Locate every blood parasite and identify its species.
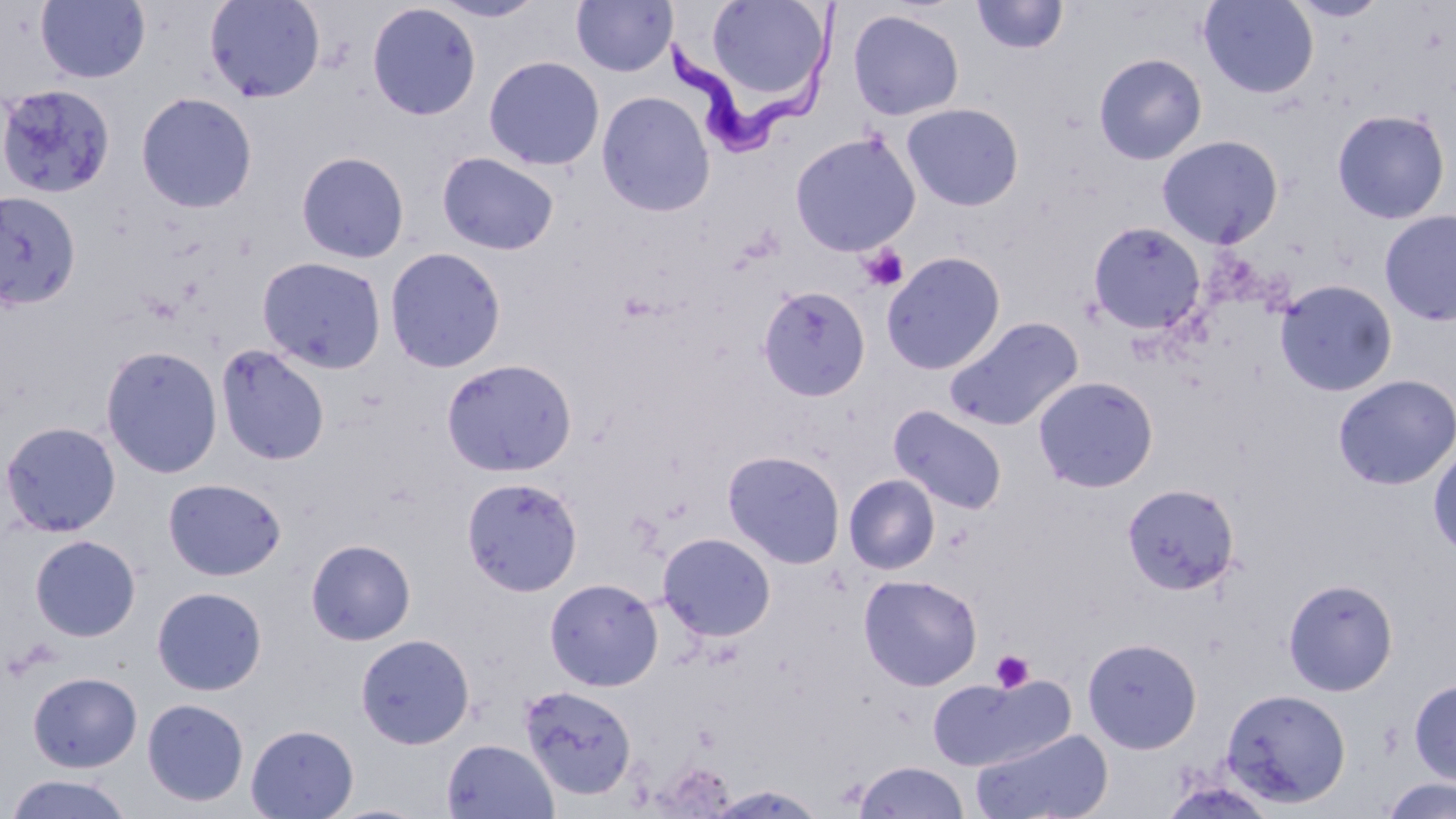

Approximate bounding boxes as (x1,y1)-(x2,y2) corner pairs in pixels.
Trypanosoma brucei: (662,2)-(849,161).
No Plasmodium falciparum, Plasmodium ovale, Plasmodium malariae, Plasmodium vivax, or Babesia divergens observed.

Summary:
  - Platelet locations: (859,244)-(909,292), (990,650)-(1034,692)
  - Uninfected red blood cell locations: (36,0)-(150,84), (204,0)-(326,103), (430,0)-(548,23), (702,0)-(831,108), (970,0)-(1069,55), (1199,0)-(1319,98), (570,1)-(676,77), (366,3)-(482,121), (846,9)-(965,121), (1093,53)-(1208,164), (484,56)-(605,171), (8,84)-(115,187), (596,91)-(716,217), (136,92)-(257,213), (901,103)-(1024,211), (1332,109)-(1450,224), (789,131)-(921,256), (1157,135)-(1283,249), (296,151)-(410,264), (436,152)-(560,256), (0,190)-(82,310), (1379,209)-(1456,326), (1087,221)-(1205,335), (384,247)-(506,373), (881,251)-(1006,375), (257,256)-(387,373), (1274,279)-(1398,397), (758,285)-(871,402), (943,317)-(1085,433), (216,343)-(331,465), (100,345)-(223,479), (440,358)-(577,476), (1332,373)-(1456,490), (1032,375)-(1159,493), (889,405)-(1008,515), (0,420)-(121,537), (1427,444)-(1456,557), (722,450)-(846,569), (843,474)-(940,575), (460,476)-(583,596), (162,478)-(286,581), (1122,483)-(1240,595), (657,532)-(776,642), (29,535)-(141,642), (306,538)-(416,646), (858,574)-(983,691), (1282,577)-(1398,696), (544,578)-(663,691), (151,586)-(267,696), (355,633)-(475,749), (1082,637)-(1202,754), (27,671)-(143,773), (925,675)-(1068,771), (1409,677)-(1456,785), (519,685)-(637,800), (1221,688)-(1351,808), (142,698)-(249,807), (245,724)-(359,818), (971,728)-(1114,819), (442,738)-(559,819), (853,761)-(970,819), (3,772)-(135,818), (1380,777)-(1456,819), (1158,779)-(1278,819), (705,785)-(827,818), (321,802)-(435,819)
  - Slide-level diagnosis: Trypanosoma brucei
  - Field of view: single
  - Preparation: thin blood film
  - Image size: 1456×819 pixels
  - Modality: light microscopy
  - Magnification: 1000x
  - Stain: May-Grünwald-Giemsa